Report the malaria status of this cell.
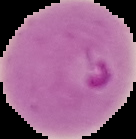
Parasitized.

From a thin blood smear. Segmented cell region on a black background. Image is 136×139 pixels.